Classify this cell by malaria status.
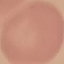

It is uninfected.

Summary:
  - Capture: smartphone through the microscope eyepiece
  - Preparation: thin smear
  - Image type: automatically extracted cell patch, resized to 64 × 64 pixels
  - Stain: Giemsa